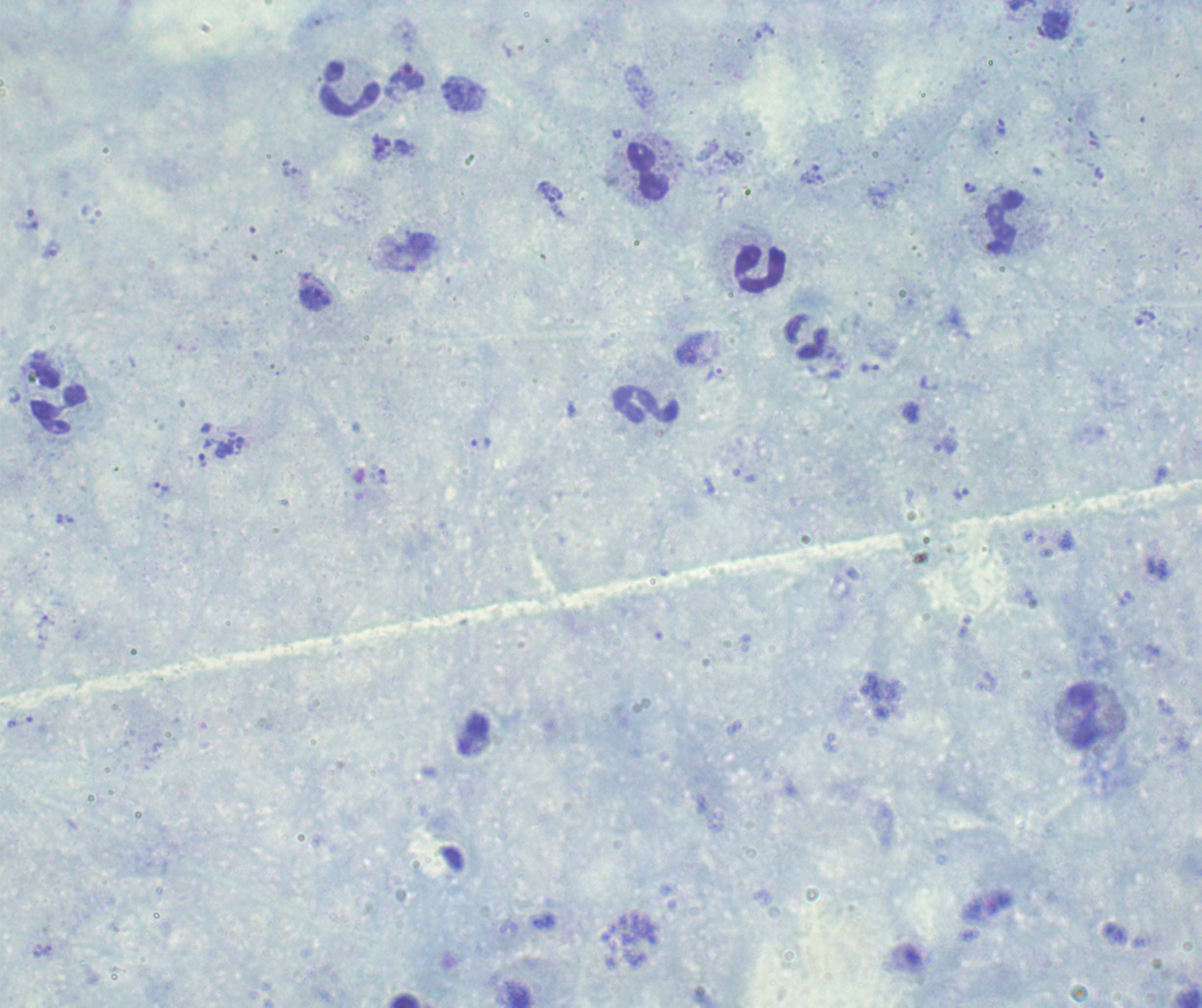
One field from this slide. Thick blood smear. Romanowsky stain. Image is 1202×1008 pixels.